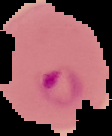 Result: Plasmodium parasites identified. From a thin blood film. Segmented cell region on a black background. Image is 112×136 pixels.